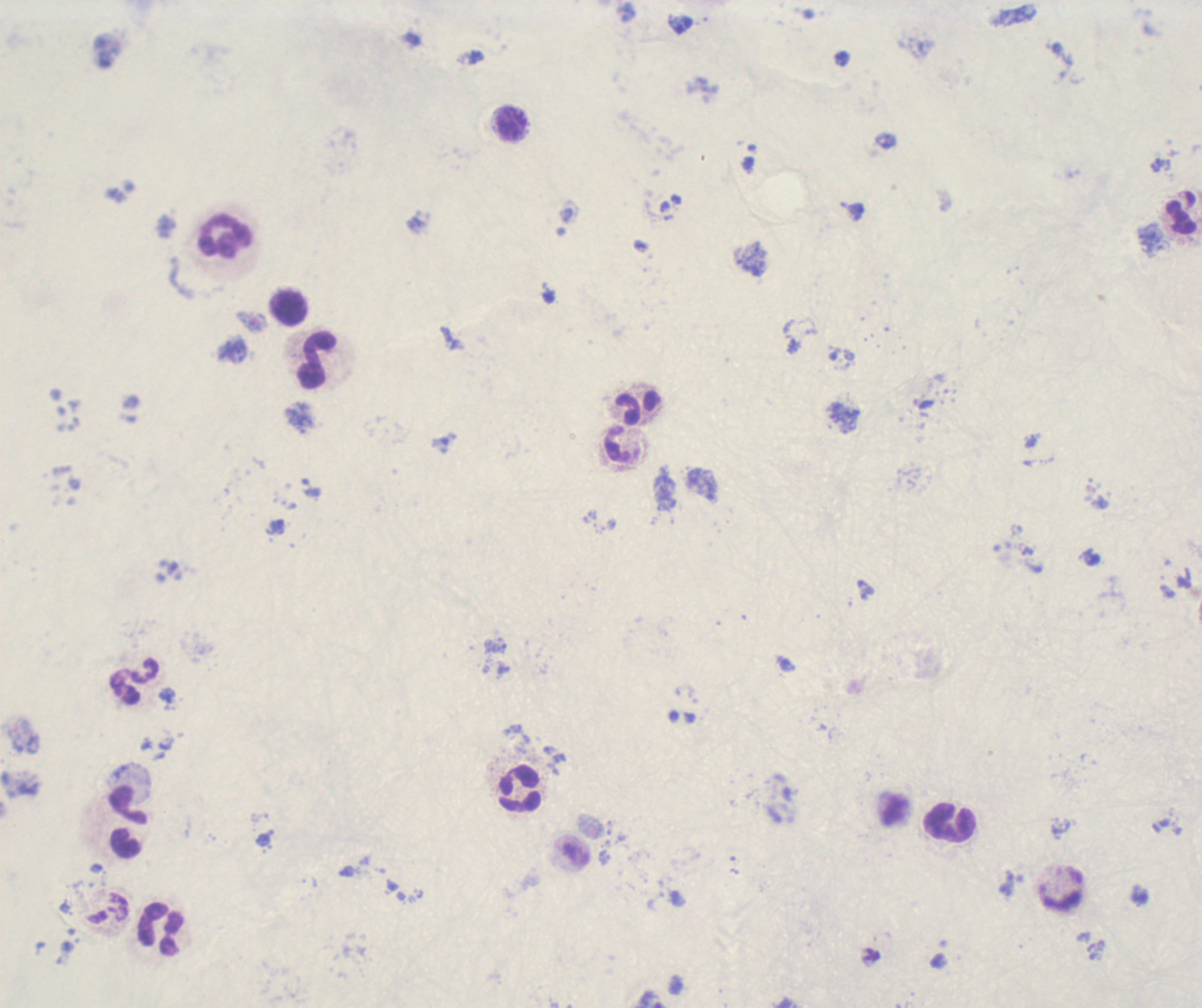

Approximate object centers, in pixels from the top-left corner. Leukocyte locations: (x=512, y=122), (x=1181, y=214), (x=225, y=237), (x=289, y=307), (x=318, y=360), (x=636, y=408), (x=617, y=445), (x=135, y=683), (x=520, y=789), (x=949, y=822), (x=126, y=844), (x=161, y=929). Trophozoite locations: (x=1161, y=164), (x=1184, y=579). Previously used in an actual diagnosis. Romanowsky stain. Image is 1202×1008 pixels. Captured at 100x magnification. Result: positive for malaria parasites. Thick blood film. Background quality: poor. Single field of view.